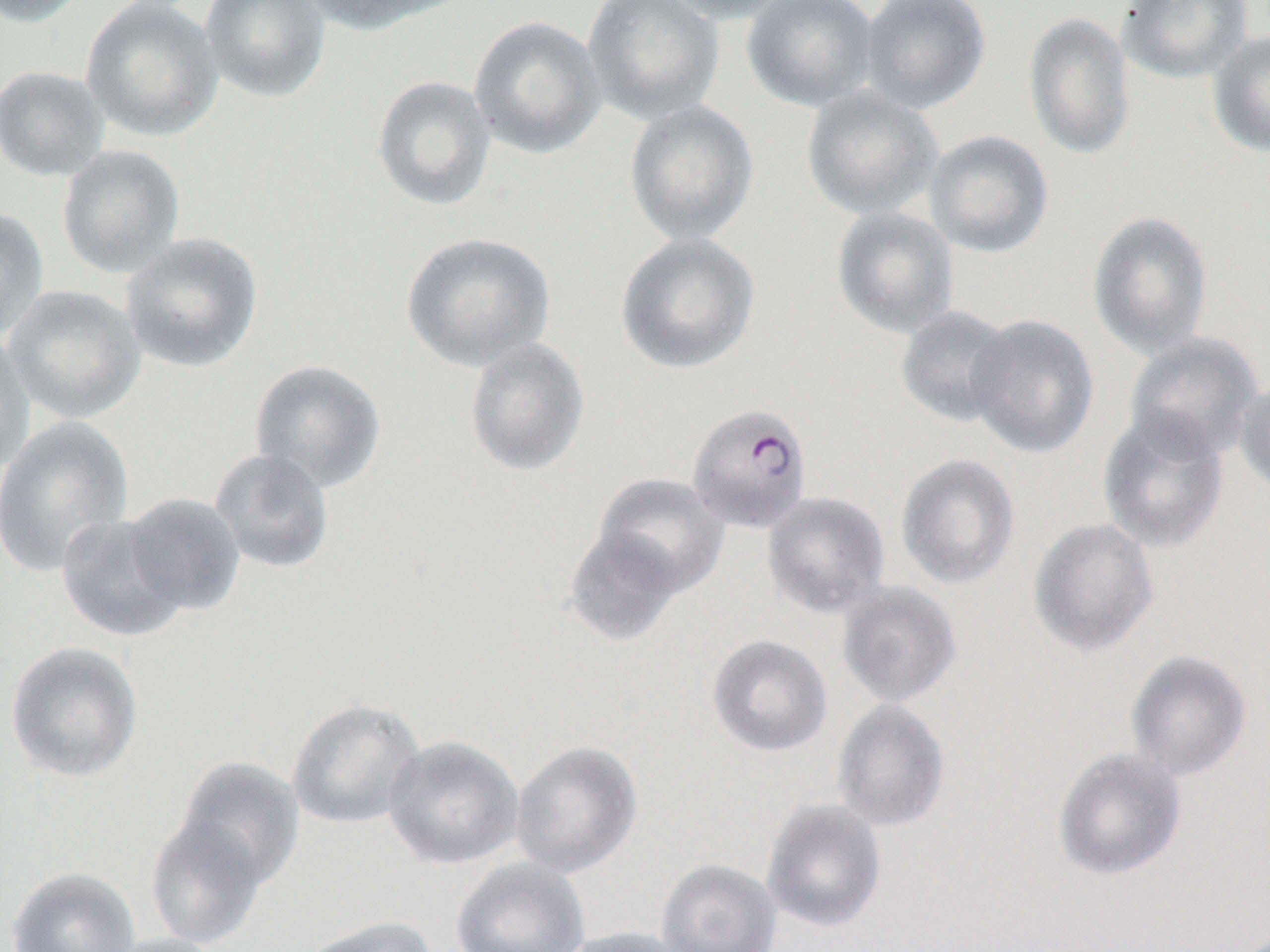
{
  "slide_level_diagnosis": "Plasmodium falciparum",
  "field_of_view": "single",
  "magnification": "1000x",
  "modality": "light microscopy",
  "plasmodium_falciparum_infected_red_blood_cell_locations": "approximate bounding boxes as named x1/y1/x2/y2 corners in pixels: (x1=686, y1=402, x2=813, y2=533)",
  "uninfected_red_blood_cell_locations": "approximate bounding boxes as named x1/y1/x2/y2 corners in pixels: (x1=0, y1=0, x2=90, y2=28), (x1=80, y1=0, x2=224, y2=142), (x1=199, y1=0, x2=332, y2=103), (x1=295, y1=0, x2=451, y2=35), (x1=581, y1=0, x2=725, y2=126), (x1=657, y1=0, x2=798, y2=23), (x1=743, y1=0, x2=881, y2=112), (x1=858, y1=0, x2=992, y2=114), (x1=1118, y1=0, x2=1253, y2=84), (x1=1023, y1=11, x2=1136, y2=160), (x1=469, y1=15, x2=607, y2=159), (x1=1206, y1=30, x2=1270, y2=157), (x1=0, y1=65, x2=110, y2=181), (x1=372, y1=75, x2=496, y2=211), (x1=801, y1=86, x2=944, y2=221), (x1=623, y1=98, x2=759, y2=247), (x1=924, y1=129, x2=1054, y2=258), (x1=56, y1=145, x2=185, y2=279), (x1=0, y1=205, x2=49, y2=343), (x1=831, y1=206, x2=960, y2=339), (x1=1087, y1=210, x2=1215, y2=360), (x1=119, y1=232, x2=264, y2=373), (x1=401, y1=232, x2=556, y2=372), (x1=615, y1=232, x2=761, y2=375), (x1=3, y1=284, x2=146, y2=424), (x1=895, y1=305, x2=1017, y2=427), (x1=966, y1=314, x2=1099, y2=459), (x1=0, y1=329, x2=37, y2=474), (x1=1123, y1=332, x2=1265, y2=462), (x1=463, y1=337, x2=590, y2=477), (x1=249, y1=360, x2=387, y2=493), (x1=1234, y1=377, x2=1270, y2=500), (x1=1097, y1=410, x2=1230, y2=554), (x1=0, y1=415, x2=135, y2=577), (x1=208, y1=448, x2=336, y2=574), (x1=895, y1=453, x2=1021, y2=590), (x1=592, y1=472, x2=729, y2=598), (x1=762, y1=491, x2=890, y2=618), (x1=120, y1=493, x2=246, y2=616), (x1=55, y1=513, x2=192, y2=642), (x1=1028, y1=517, x2=1160, y2=657), (x1=562, y1=526, x2=687, y2=647), (x1=837, y1=581, x2=963, y2=708), (x1=706, y1=634, x2=833, y2=757), (x1=4, y1=641, x2=143, y2=783), (x1=1125, y1=649, x2=1253, y2=782), (x1=286, y1=698, x2=425, y2=830), (x1=831, y1=699, x2=950, y2=833), (x1=383, y1=735, x2=524, y2=870), (x1=510, y1=740, x2=643, y2=878), (x1=1053, y1=746, x2=1187, y2=881), (x1=174, y1=757, x2=305, y2=892), (x1=761, y1=798, x2=887, y2=933), (x1=145, y1=813, x2=269, y2=950), (x1=451, y1=857, x2=590, y2=951), (x1=656, y1=858, x2=782, y2=952), (x1=6, y1=867, x2=141, y2=952), (x1=297, y1=915, x2=438, y2=952), (x1=555, y1=926, x2=693, y2=952), (x1=99, y1=933, x2=231, y2=952)",
  "preparation": "thin blood smear",
  "image_size": "1270×952 pixels"
}